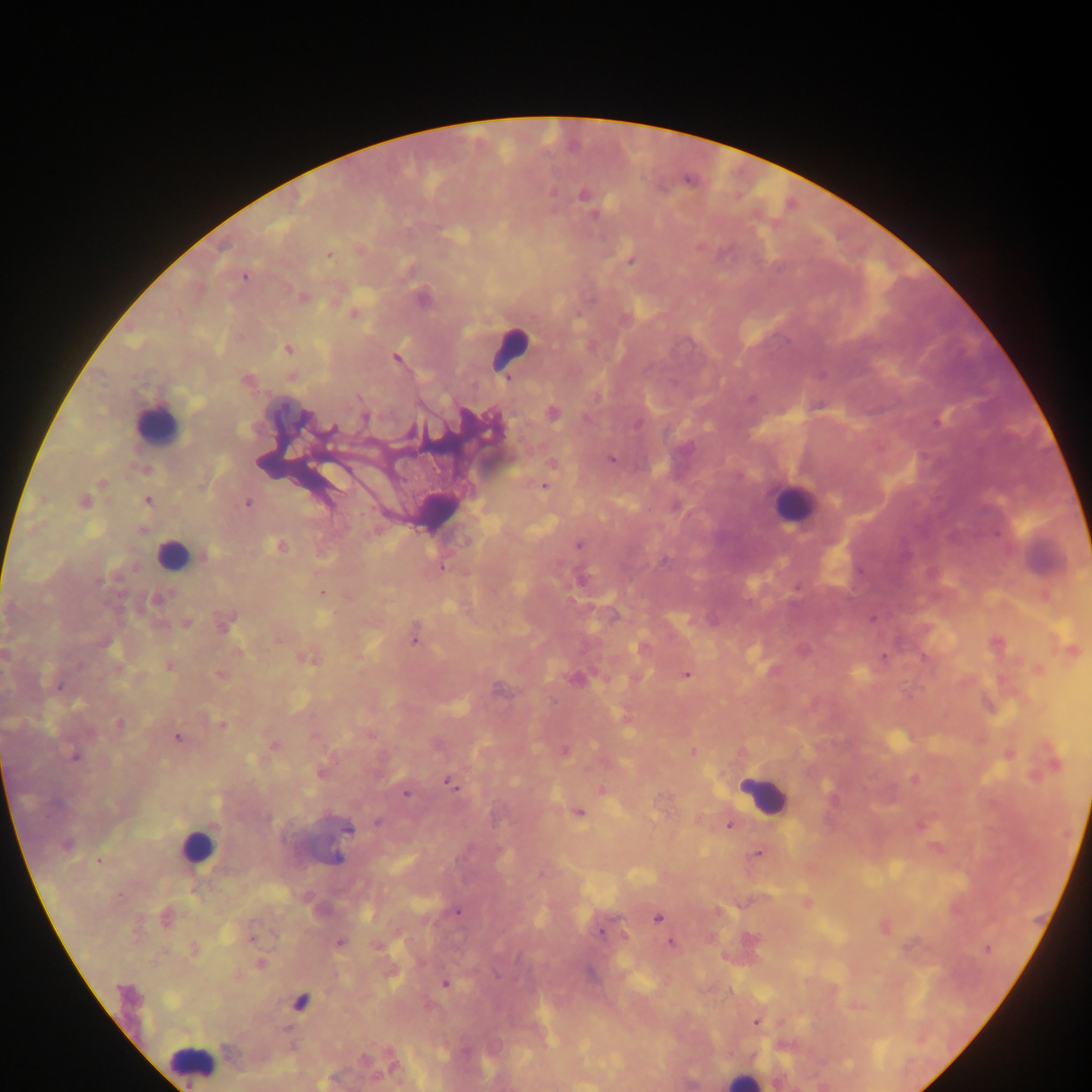

preparation = thick blood smear
field of view = single
Plasmodium parasite locations = approximate centers as x y in pixels: 687 181; 776 226; 329 256; 633 261; 245 277; 288 347; 395 357; 506 379; 245 380; 366 417; 331 428; 611 459; 312 465; 101 483; 543 486; 42 500; 84 500; 146 500; 249 502; 577 545; 441 565; 322 592; 872 619; 413 640; 882 656; 686 674; 61 687; 177 738; 564 750; 693 751; 75 756; 914 780; 448 783; 406 794; 579 813; 729 824; 918 825; 757 853; 99 861; 458 911; 658 919; 602 932; 625 936; 252 940; 671 942; 259 963; 445 983; 755 1021
capture = mobile-phone photograph through a microscope
leukocyte locations = approximate centers as x y in pixels: 516 346; 156 426; 794 512; 173 557; 762 788; 204 845; 189 1060
image size = 1092×1092 pixels
country = Ghana